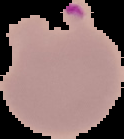
Summary:
  - Preparation: thin blood film
  - Image type: segmented cell region on a black background
  - Result: malaria parasites detected
  - Image size: 124×139 pixels